Name the parasite shown.
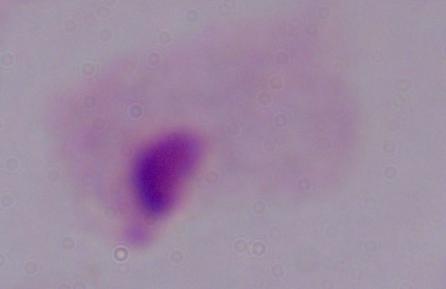
A trichomonad.

magnification = 1000x
modality = photomicrograph